State which parasite is depicted.
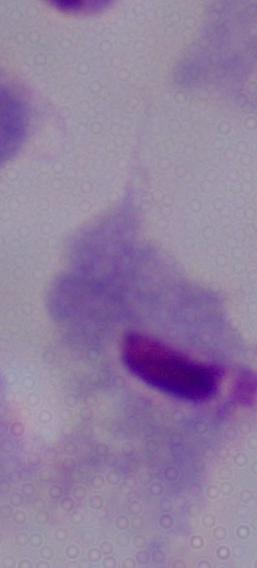

This is a trichomonad.

Captured at 1000x magnification. Photomicrograph.